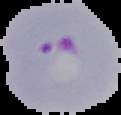

Summary:
  - Preparation: thin blood film
  - Image type: segmented cell region on a black background
  - Image size: 121×115 pixels
  - Malaria status: parasitized